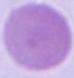

{
  "identification": "red blood cell",
  "modality": "micrograph",
  "magnification": "1000x"
}